Assess this cell for malaria.
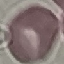
It is uninfected.

Giemsa stain. Photographed with a smartphone camera at the microscope eyepiece. Thin blood film. Automatically extracted cell patch, resized to 64 × 64 pixels.